State which parasite is depicted.
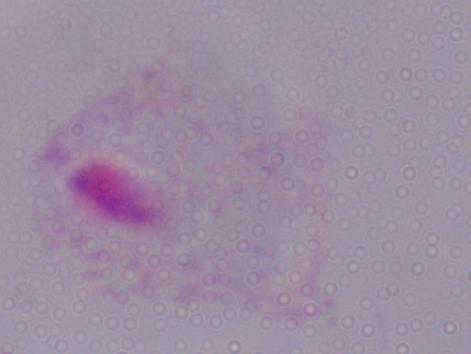

A trichomonad.

1000x magnification. Photomicrograph.